Assess the morphology of the erythrocytes.
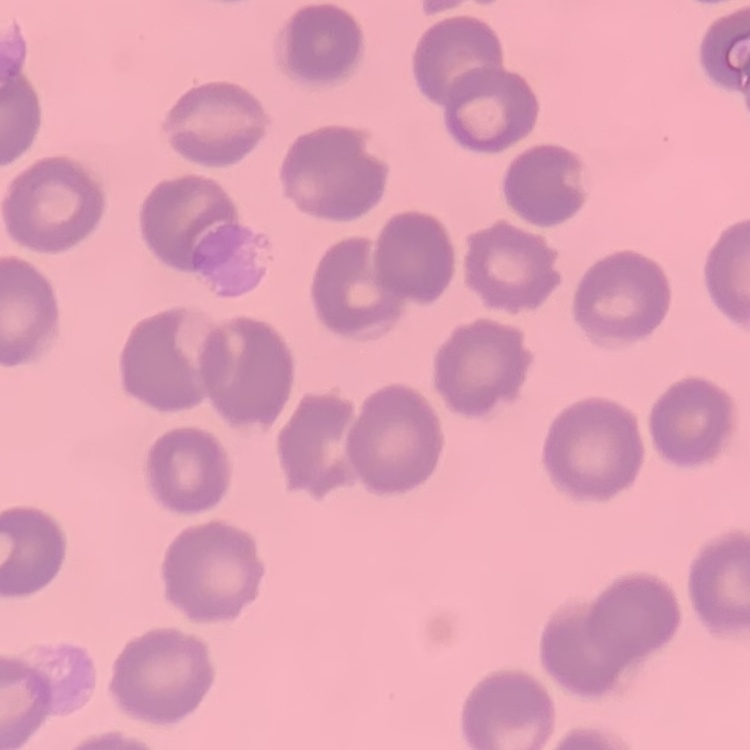
They show no rouleaux formation.

Thin blood smear. Field's or Giemsa stain. One tile cut from a larger photomicrograph.